Locate every Plasmodium falciparum-infected red blood cell.
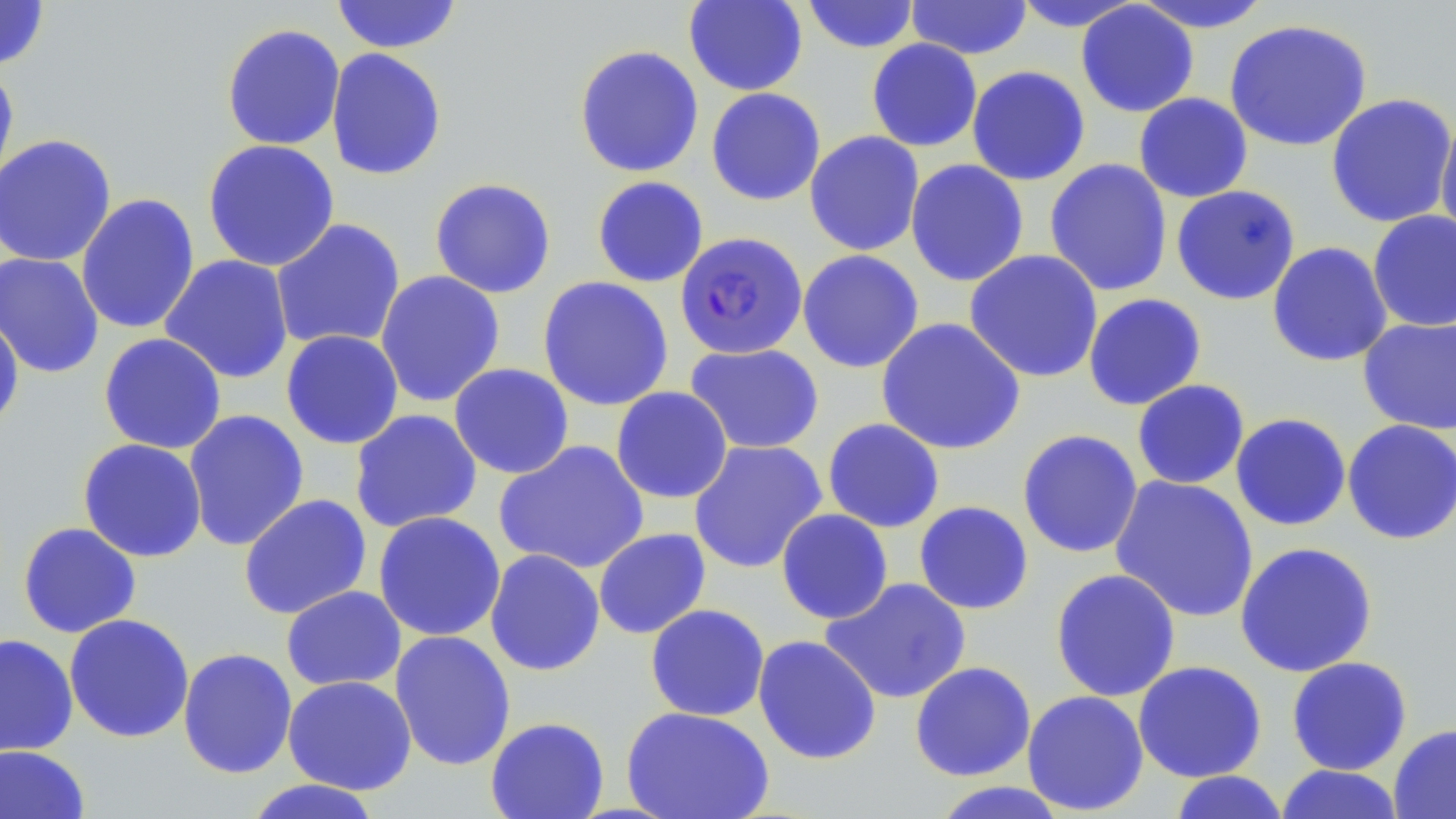
Approximate bounding boxes as named x1/y1/x2/y2 corners in pixels.
Plasmodium falciparum-infected red blood cells: (x1=675, y1=231, x2=808, y2=360).

Uninfected red blood cell locations: (x1=0, y1=0, x2=50, y2=70), (x1=331, y1=0, x2=463, y2=54), (x1=683, y1=0, x2=808, y2=96), (x1=801, y1=0, x2=921, y2=54), (x1=905, y1=0, x2=1033, y2=60), (x1=1130, y1=0, x2=1276, y2=33), (x1=1009, y1=1, x2=1145, y2=32), (x1=1075, y1=2, x2=1199, y2=118), (x1=1223, y1=18, x2=1373, y2=152), (x1=221, y1=23, x2=346, y2=151), (x1=866, y1=38, x2=983, y2=152), (x1=573, y1=44, x2=704, y2=178), (x1=325, y1=48, x2=447, y2=181), (x1=0, y1=61, x2=19, y2=196), (x1=966, y1=65, x2=1091, y2=186), (x1=706, y1=87, x2=826, y2=206), (x1=1133, y1=92, x2=1253, y2=203), (x1=1325, y1=93, x2=1455, y2=228), (x1=1434, y1=110, x2=1456, y2=246), (x1=804, y1=130, x2=925, y2=256), (x1=0, y1=133, x2=117, y2=268), (x1=202, y1=139, x2=340, y2=272), (x1=905, y1=158, x2=1030, y2=287), (x1=1044, y1=158, x2=1173, y2=297), (x1=592, y1=175, x2=709, y2=288), (x1=428, y1=177, x2=557, y2=299), (x1=1171, y1=185, x2=1301, y2=305), (x1=76, y1=193, x2=200, y2=335), (x1=1367, y1=210, x2=1456, y2=332), (x1=270, y1=218, x2=406, y2=351), (x1=1267, y1=241, x2=1393, y2=367), (x1=797, y1=249, x2=925, y2=373), (x1=964, y1=249, x2=1104, y2=383), (x1=1, y1=251, x2=104, y2=379), (x1=159, y1=254, x2=294, y2=384), (x1=375, y1=270, x2=506, y2=407), (x1=536, y1=275, x2=674, y2=411), (x1=1083, y1=292, x2=1207, y2=411), (x1=0, y1=311, x2=25, y2=433), (x1=875, y1=317, x2=1026, y2=456), (x1=1358, y1=317, x2=1456, y2=436), (x1=280, y1=330, x2=404, y2=450), (x1=98, y1=332, x2=227, y2=454), (x1=684, y1=342, x2=825, y2=454), (x1=448, y1=363, x2=575, y2=480), (x1=1132, y1=379, x2=1250, y2=490), (x1=610, y1=386, x2=732, y2=503), (x1=349, y1=408, x2=483, y2=533), (x1=183, y1=409, x2=310, y2=552), (x1=1230, y1=412, x2=1352, y2=531), (x1=822, y1=418, x2=945, y2=533), (x1=1341, y1=419, x2=1456, y2=545), (x1=1016, y1=429, x2=1144, y2=559), (x1=77, y1=438, x2=208, y2=563), (x1=494, y1=439, x2=650, y2=575), (x1=688, y1=440, x2=827, y2=573), (x1=1109, y1=475, x2=1259, y2=623), (x1=238, y1=494, x2=372, y2=619), (x1=913, y1=500, x2=1035, y2=615), (x1=775, y1=508, x2=894, y2=624), (x1=373, y1=511, x2=506, y2=642), (x1=17, y1=521, x2=142, y2=638), (x1=593, y1=528, x2=711, y2=639), (x1=1234, y1=541, x2=1378, y2=678), (x1=484, y1=548, x2=605, y2=676), (x1=1050, y1=568, x2=1181, y2=702), (x1=819, y1=577, x2=972, y2=704), (x1=281, y1=585, x2=407, y2=692), (x1=645, y1=603, x2=770, y2=722), (x1=63, y1=613, x2=195, y2=743), (x1=390, y1=630, x2=516, y2=771), (x1=0, y1=633, x2=79, y2=758), (x1=752, y1=635, x2=882, y2=764), (x1=177, y1=647, x2=298, y2=779), (x1=1286, y1=656, x2=1413, y2=776), (x1=1132, y1=660, x2=1267, y2=783), (x1=909, y1=661, x2=1037, y2=782), (x1=282, y1=675, x2=417, y2=795), (x1=1022, y1=690, x2=1150, y2=816), (x1=621, y1=706, x2=774, y2=818), (x1=485, y1=716, x2=610, y2=819), (x1=1388, y1=724, x2=1456, y2=819), (x1=0, y1=745, x2=91, y2=819), (x1=1274, y1=764, x2=1406, y2=819), (x1=1167, y1=771, x2=1291, y2=819), (x1=241, y1=779, x2=385, y2=819), (x1=927, y1=781, x2=1073, y2=819). Slide-level diagnosis: Plasmodium falciparum. Light microscopy. One field of a larger specimen. Thin blood film. May-Grünwald-Giemsa stain. Image is 1456×819 pixels. 1000x magnification.